Assess the morphology of the erythrocytes.
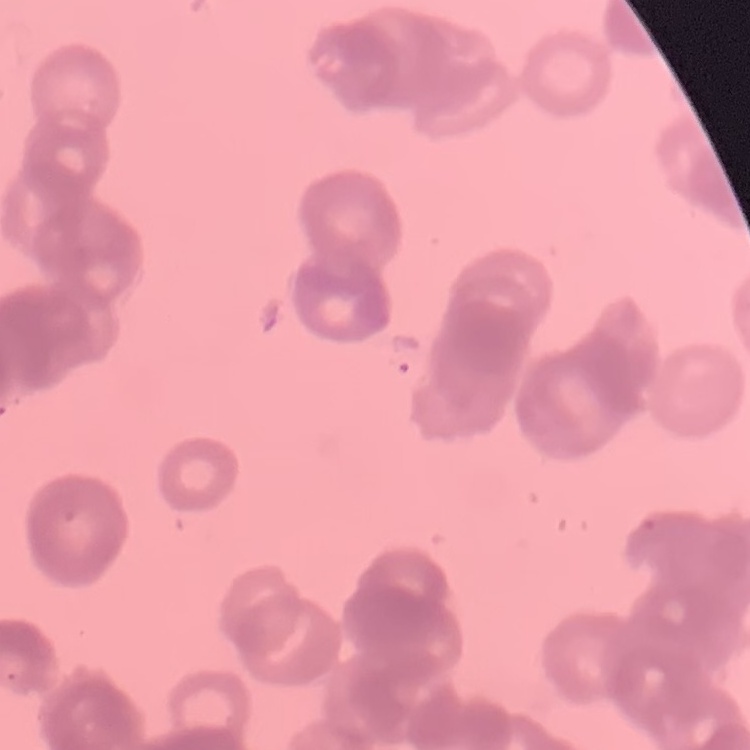

They show rouleaux formation.

Thin blood film. Stained with either Field's or Giemsa. Square crop of a larger photomicrograph.